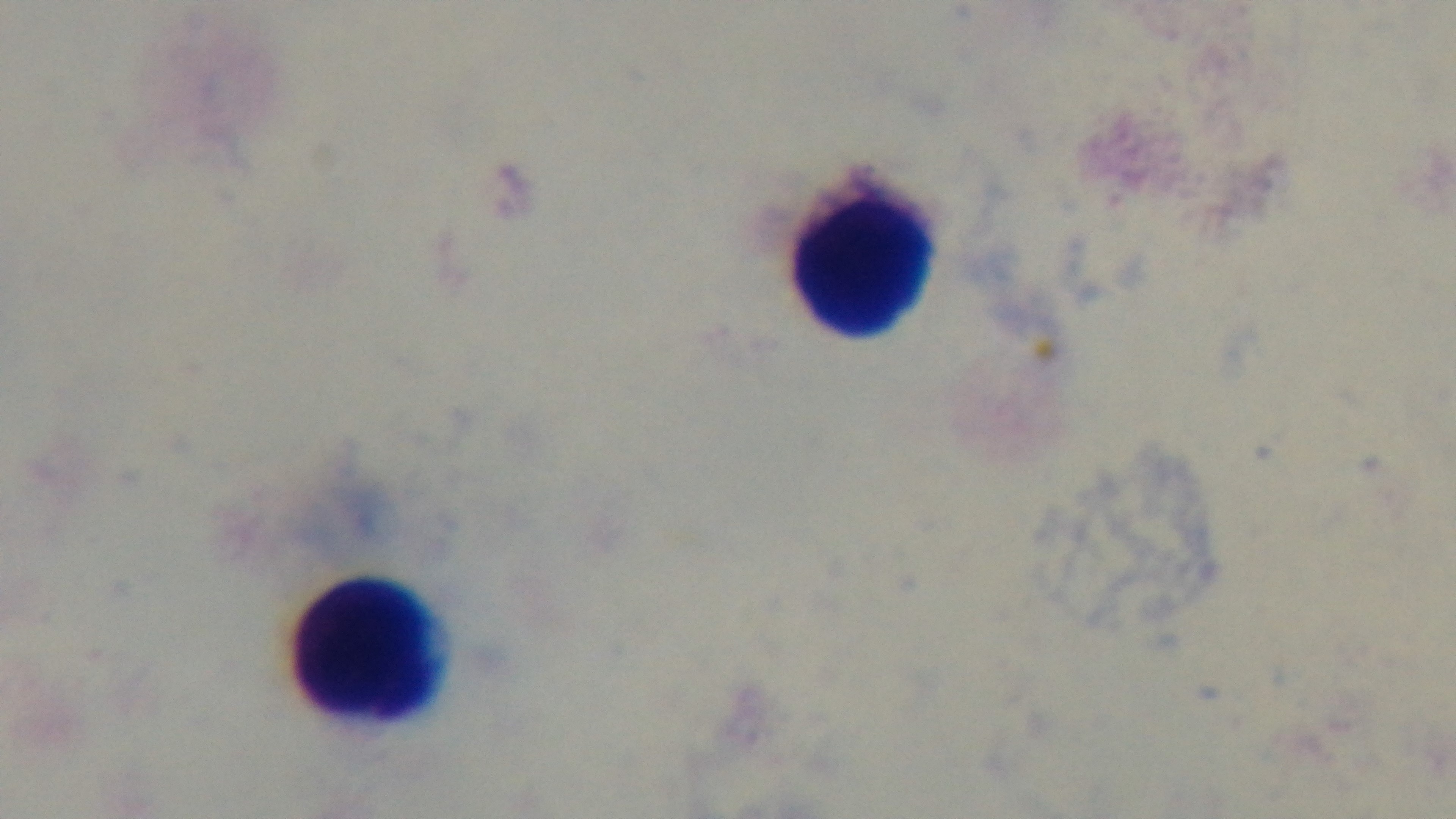

Summary:
  - Stain: Giemsa
  - Modality: light microscopy
  - Capture: mounted 4K digital camera
  - Preparation: thick smear
  - Objective: 100x oil immersion
  - Malaria status: negative
  - Field of view: single